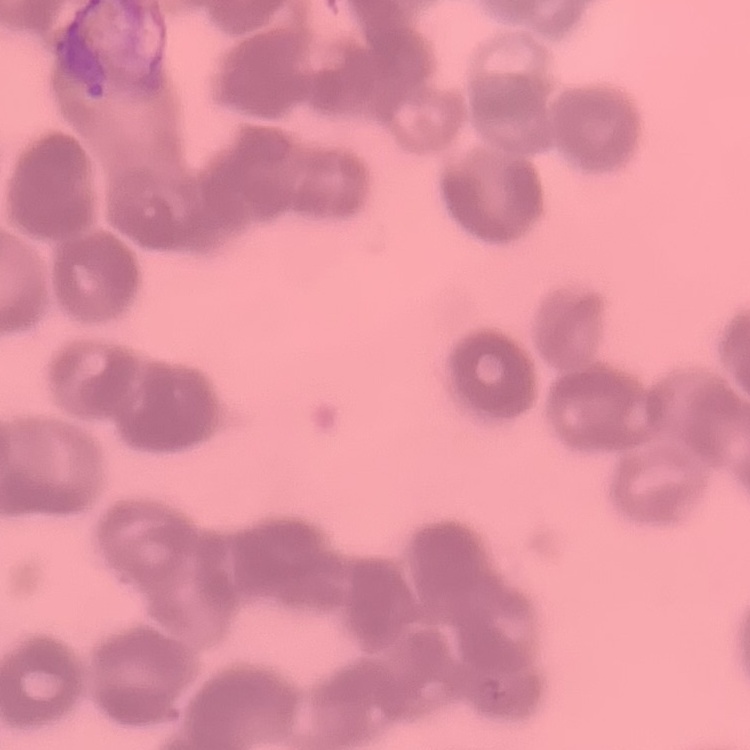

The red blood cells show rouleaux formation. One tile cut from a larger photomicrograph. Thin blood smear. Stained with either Field's or Giemsa.